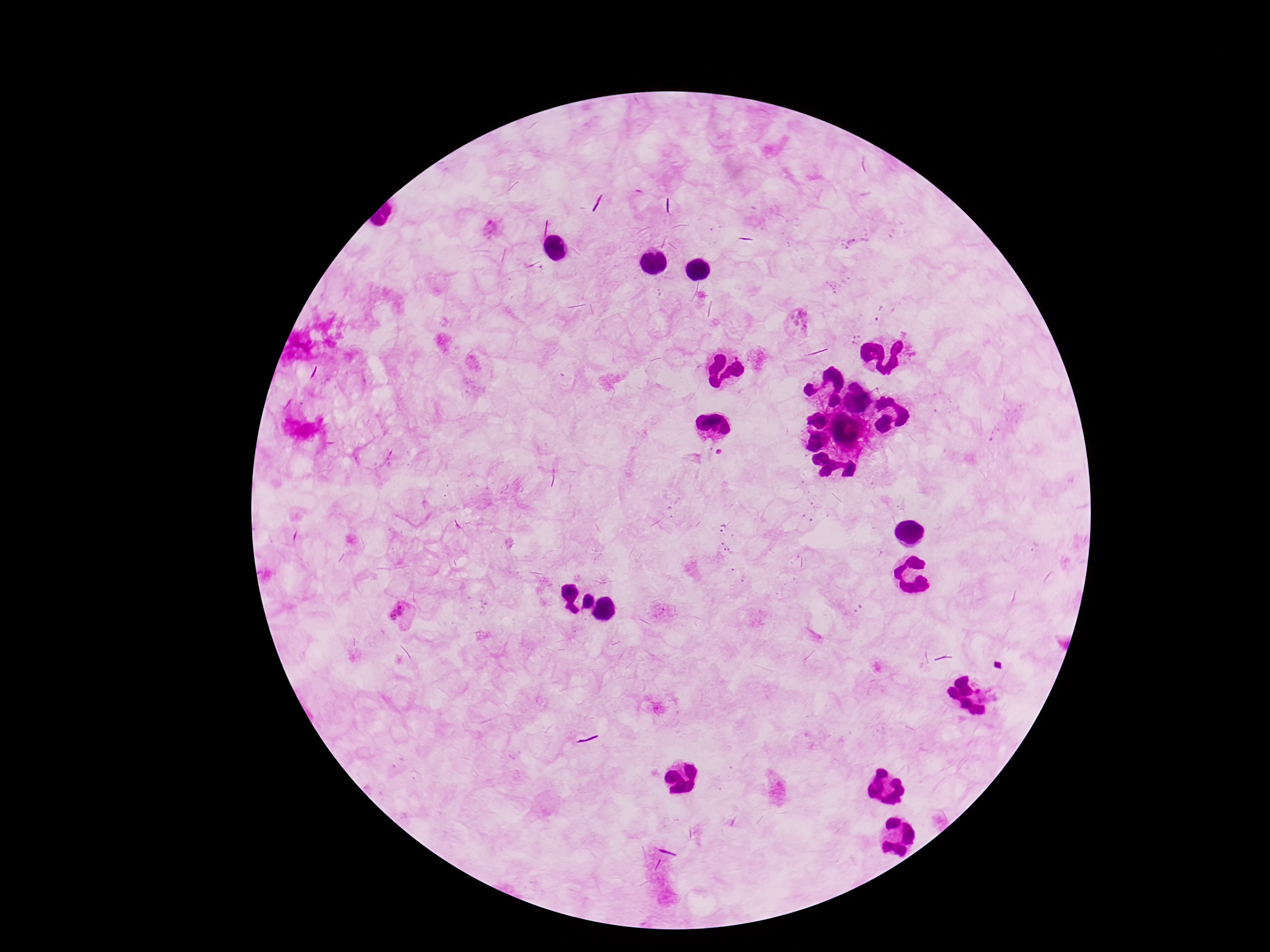

{
  "patient_malaria_status": "positive",
  "stain": "Giemsa",
  "field_of_view": "single",
  "magnification": "100x",
  "plasmodium_parasite_locations": "approximate centers as {x, y} in pixels: {494, 230}, {798, 321}, {403, 617}",
  "image_size": "1270×952 pixels",
  "preparation": "thick peripheral-blood smear",
  "capture": "smartphone camera through the microscope eyepiece"
}